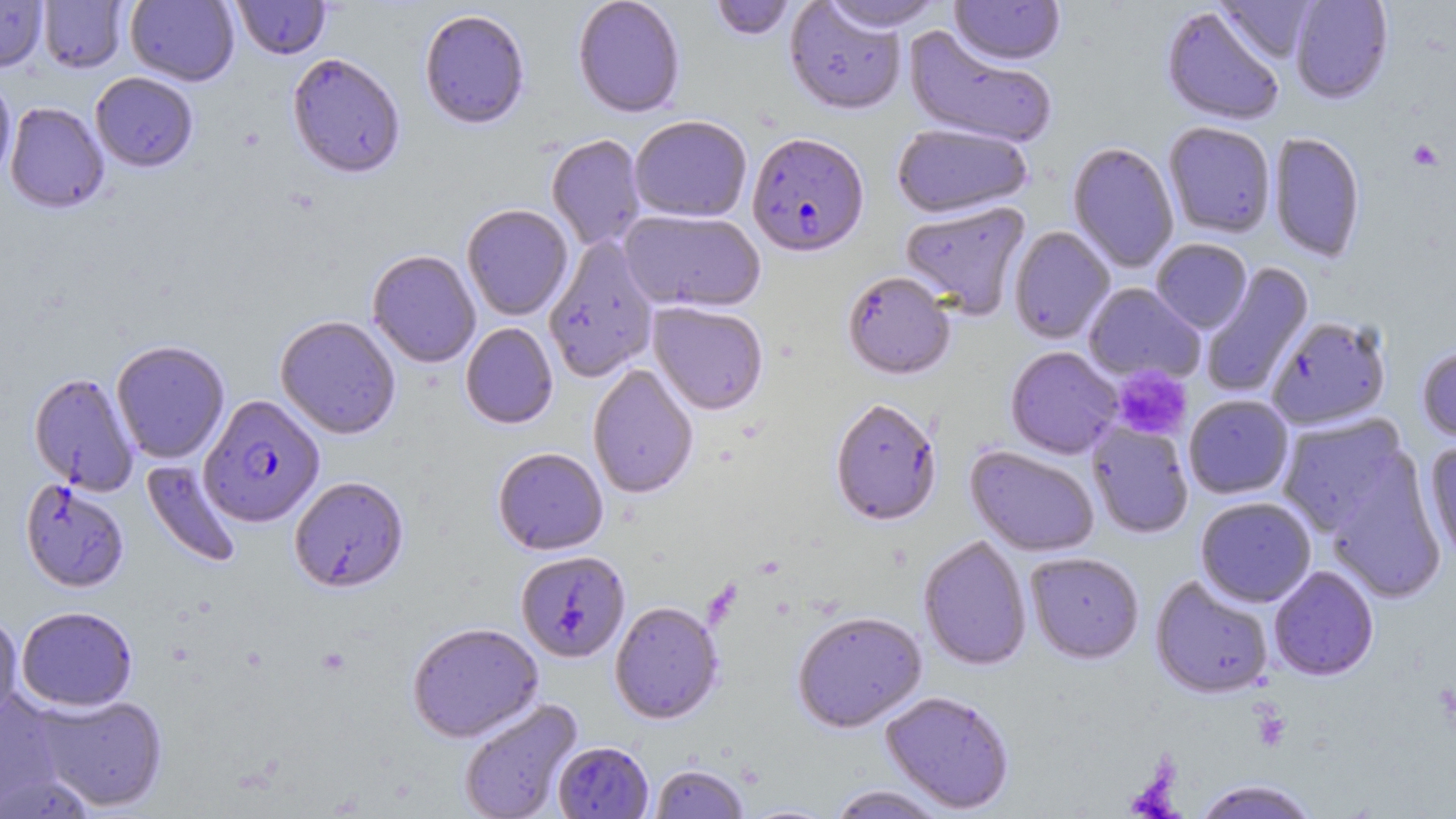 Approximate bounding boxes as named x1/y1/x2/y2 corners in pixels. Uninfected red blood cell locations: (x1=0, y1=0, x2=48, y2=72), (x1=125, y1=0, x2=239, y2=86), (x1=231, y1=0, x2=332, y2=60), (x1=572, y1=0, x2=686, y2=118), (x1=708, y1=0, x2=797, y2=42), (x1=949, y1=0, x2=1065, y2=66), (x1=1289, y1=0, x2=1393, y2=104), (x1=38, y1=1, x2=128, y2=73), (x1=784, y1=1, x2=907, y2=115), (x1=818, y1=1, x2=946, y2=34), (x1=1215, y1=1, x2=1319, y2=64), (x1=1161, y1=6, x2=1285, y2=127), (x1=419, y1=8, x2=530, y2=129), (x1=904, y1=26, x2=1057, y2=149), (x1=286, y1=52, x2=405, y2=179), (x1=0, y1=71, x2=16, y2=184), (x1=90, y1=72, x2=198, y2=172), (x1=5, y1=102, x2=109, y2=214), (x1=629, y1=115, x2=752, y2=222), (x1=1163, y1=122, x2=1276, y2=238), (x1=891, y1=123, x2=1033, y2=219), (x1=1268, y1=132, x2=1365, y2=263), (x1=546, y1=134, x2=646, y2=252), (x1=1067, y1=141, x2=1179, y2=273), (x1=900, y1=201, x2=1031, y2=319), (x1=462, y1=204, x2=573, y2=321), (x1=619, y1=209, x2=766, y2=313), (x1=1008, y1=226, x2=1115, y2=344), (x1=544, y1=236, x2=659, y2=382), (x1=1151, y1=239, x2=1252, y2=333), (x1=367, y1=249, x2=481, y2=368), (x1=1199, y1=262, x2=1314, y2=399), (x1=842, y1=271, x2=955, y2=379), (x1=1083, y1=283, x2=1204, y2=384), (x1=648, y1=301, x2=769, y2=415), (x1=275, y1=315, x2=401, y2=439), (x1=1266, y1=316, x2=1392, y2=430), (x1=460, y1=323, x2=558, y2=429), (x1=112, y1=339, x2=230, y2=464), (x1=1416, y1=343, x2=1456, y2=444), (x1=1005, y1=346, x2=1123, y2=459), (x1=587, y1=364, x2=699, y2=499), (x1=27, y1=372, x2=140, y2=495), (x1=1183, y1=395, x2=1294, y2=499), (x1=829, y1=396, x2=942, y2=526), (x1=1275, y1=414, x2=1410, y2=535), (x1=1087, y1=421, x2=1194, y2=539), (x1=1424, y1=440, x2=1456, y2=564), (x1=965, y1=445, x2=1100, y2=557), (x1=492, y1=447, x2=608, y2=555), (x1=1324, y1=458, x2=1447, y2=603), (x1=141, y1=459, x2=242, y2=569), (x1=289, y1=476, x2=409, y2=592), (x1=20, y1=479, x2=129, y2=593), (x1=1195, y1=496, x2=1316, y2=607), (x1=917, y1=534, x2=1032, y2=671), (x1=515, y1=550, x2=630, y2=663), (x1=1025, y1=551, x2=1145, y2=664), (x1=1268, y1=565, x2=1379, y2=681), (x1=1150, y1=575, x2=1273, y2=699), (x1=609, y1=600, x2=724, y2=724), (x1=16, y1=606, x2=138, y2=712), (x1=792, y1=611, x2=927, y2=732), (x1=0, y1=613, x2=23, y2=727), (x1=407, y1=621, x2=543, y2=742), (x1=0, y1=690, x2=70, y2=813), (x1=880, y1=690, x2=1015, y2=813), (x1=31, y1=692, x2=168, y2=812), (x1=458, y1=698, x2=582, y2=819), (x1=552, y1=741, x2=653, y2=818), (x1=650, y1=763, x2=750, y2=819), (x1=1191, y1=779, x2=1322, y2=819), (x1=824, y1=785, x2=950, y2=818), (x1=739, y1=802, x2=840, y2=818). Platelet locations: (x1=1407, y1=139, x2=1445, y2=171), (x1=1110, y1=366, x2=1192, y2=442). Plasmodium falciparum-infected red blood cell locations: (x1=747, y1=131, x2=870, y2=256), (x1=199, y1=394, x2=325, y2=528). Slide-level diagnosis: Plasmodium falciparum. Captured at 1000x magnification. Single field of view. Optical microscopy. Image is 1456×819 pixels. Thin blood smear. May-Grünwald-Giemsa stain.